Name the blood parasite species.
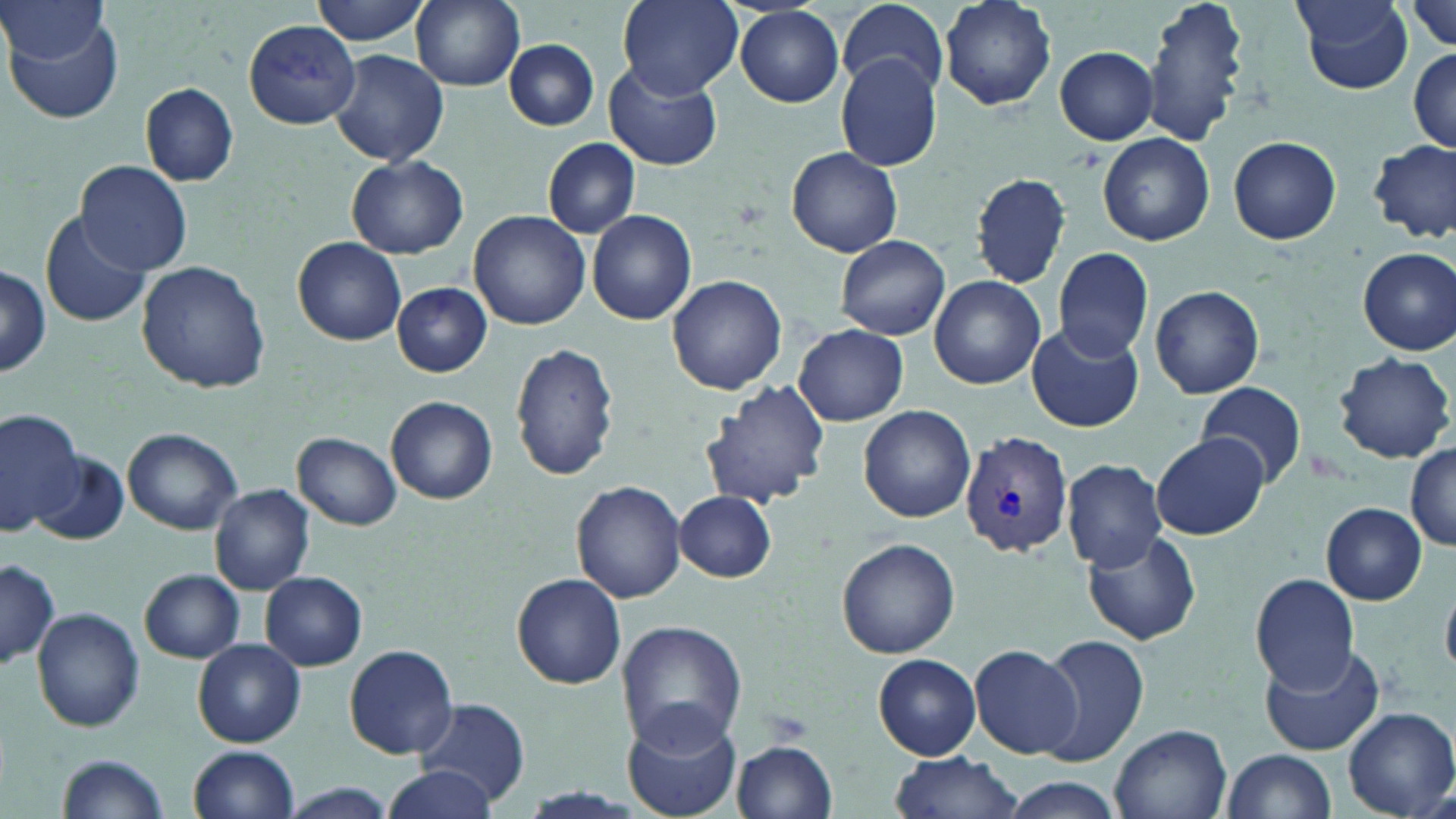
Plasmodium vivax.

modality = optical microscopy
Plasmodium vivax-infected red blood cell locations = approximate bounding boxes as (x1, y1, x2, y2) in pixels: (960, 432, 1074, 556)
preparation = thin blood film
magnification = 1000x
stain = May-Grünwald-Giemsa
image size = 1456×819 pixels
uninfected red blood cell locations = approximate bounding boxes as (x1, y1, x2, y2) in pixels: (1, 0, 110, 68), (315, 0, 434, 46), (411, 0, 525, 91), (618, 0, 742, 99), (940, 0, 1059, 110), (1140, 0, 1251, 149), (1294, 1, 1414, 93), (1408, 1, 1456, 54), (838, 5, 948, 92), (736, 6, 846, 107), (1, 13, 125, 127), (244, 19, 362, 129), (505, 39, 599, 130), (1053, 46, 1159, 144), (329, 48, 449, 169), (1408, 48, 1456, 154), (836, 54, 942, 171), (606, 60, 723, 171), (139, 81, 239, 187), (1098, 133, 1213, 246), (1227, 135, 1341, 244), (542, 137, 641, 238), (1370, 142, 1454, 245), (786, 147, 901, 256), (346, 156, 469, 258), (77, 160, 190, 274), (970, 173, 1073, 286), (469, 209, 591, 329), (588, 210, 697, 326), (41, 211, 151, 329), (294, 236, 407, 346), (835, 236, 950, 340), (1052, 247, 1154, 361), (1358, 247, 1456, 355), (136, 260, 271, 395), (0, 265, 51, 379), (931, 273, 1046, 389), (666, 274, 786, 394), (391, 281, 492, 377), (1149, 284, 1264, 400), (1027, 322, 1143, 433), (794, 324, 909, 425), (511, 342, 619, 482), (1332, 352, 1454, 463), (701, 379, 830, 511), (1196, 381, 1307, 488), (386, 396, 498, 505), (859, 405, 974, 524), (0, 406, 84, 537), (122, 428, 243, 534), (293, 433, 403, 530), (1152, 434, 1269, 541), (1406, 443, 1456, 549), (32, 450, 129, 547), (1061, 459, 1167, 571), (570, 481, 686, 605), (210, 484, 313, 596), (677, 491, 776, 581), (1320, 503, 1427, 604), (1079, 529, 1202, 647), (837, 538, 961, 659), (1, 558, 59, 669), (139, 569, 246, 663), (260, 571, 367, 671), (513, 574, 627, 688), (1250, 574, 1360, 691), (32, 606, 144, 731), (615, 621, 745, 748), (1040, 634, 1149, 766), (193, 639, 305, 747), (341, 645, 460, 759), (971, 645, 1083, 760), (1259, 646, 1386, 757), (874, 654, 982, 760), (414, 697, 531, 808), (1340, 706, 1455, 819), (621, 709, 741, 818), (1110, 725, 1231, 819), (732, 738, 838, 819), (188, 745, 300, 819), (1220, 749, 1336, 819), (57, 752, 173, 818), (888, 753, 1024, 819), (383, 763, 498, 819), (1003, 777, 1123, 819), (282, 782, 395, 819)
field of view = one of a larger specimen